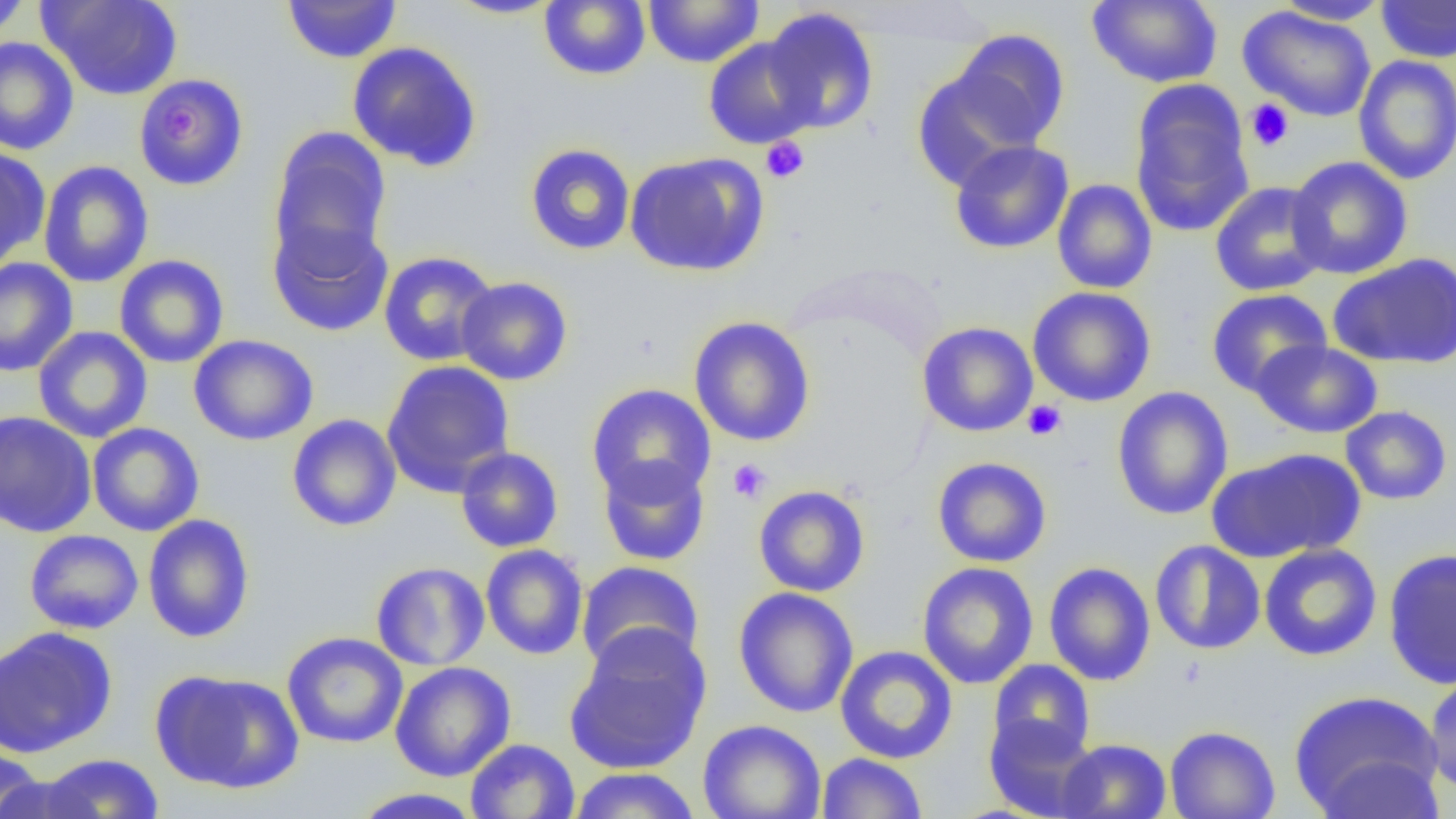

slide-level diagnosis = negative for blood parasites
magnification = 1000x
image size = 1456×819 pixels
field of view = one of a larger specimen
modality = optical microscopy
preparation = thin blood smear
platelet locations = approximate bounding boxes as named x1/y1/x2/y2 corners in pixels: (x1=1245, y1=99, x2=1295, y2=151), (x1=159, y1=104, x2=209, y2=140), (x1=761, y1=136, x2=810, y2=184), (x1=1023, y1=400, x2=1067, y2=441), (x1=727, y1=459, x2=773, y2=504)
uninfected red blood cell locations = approximate bounding boxes as named x1/y1/x2/y2 corners in pixels: (x1=0, y1=0, x2=32, y2=40), (x1=40, y1=0, x2=182, y2=101), (x1=445, y1=0, x2=562, y2=19), (x1=643, y1=0, x2=764, y2=67), (x1=1087, y1=0, x2=1223, y2=88), (x1=1273, y1=0, x2=1392, y2=25), (x1=1375, y1=0, x2=1456, y2=62), (x1=282, y1=1, x2=403, y2=64), (x1=539, y1=1, x2=651, y2=81), (x1=1238, y1=6, x2=1377, y2=122), (x1=762, y1=7, x2=880, y2=134), (x1=949, y1=29, x2=1071, y2=149), (x1=0, y1=37, x2=79, y2=155), (x1=703, y1=37, x2=817, y2=149), (x1=347, y1=41, x2=483, y2=172), (x1=1352, y1=55, x2=1456, y2=185), (x1=912, y1=67, x2=1037, y2=190), (x1=134, y1=73, x2=249, y2=191), (x1=1129, y1=82, x2=1255, y2=237), (x1=267, y1=125, x2=392, y2=270), (x1=949, y1=139, x2=1074, y2=254), (x1=524, y1=143, x2=636, y2=255), (x1=0, y1=148, x2=51, y2=267), (x1=624, y1=152, x2=768, y2=277), (x1=1286, y1=156, x2=1414, y2=279), (x1=38, y1=160, x2=154, y2=288), (x1=1052, y1=178, x2=1157, y2=294), (x1=1210, y1=181, x2=1330, y2=297), (x1=267, y1=218, x2=394, y2=338), (x1=378, y1=251, x2=500, y2=366), (x1=1329, y1=253, x2=1456, y2=369), (x1=114, y1=254, x2=230, y2=368), (x1=0, y1=257, x2=79, y2=376), (x1=455, y1=276, x2=573, y2=386), (x1=1028, y1=286, x2=1156, y2=407), (x1=1206, y1=288, x2=1333, y2=397), (x1=688, y1=316, x2=816, y2=447), (x1=917, y1=321, x2=1038, y2=437), (x1=32, y1=326, x2=153, y2=443), (x1=189, y1=335, x2=318, y2=445), (x1=1251, y1=340, x2=1383, y2=439), (x1=381, y1=360, x2=516, y2=497), (x1=586, y1=383, x2=716, y2=503), (x1=1112, y1=386, x2=1234, y2=520), (x1=1340, y1=405, x2=1453, y2=505), (x1=0, y1=410, x2=97, y2=538), (x1=286, y1=414, x2=402, y2=531), (x1=87, y1=422, x2=204, y2=536), (x1=455, y1=447, x2=564, y2=553), (x1=1207, y1=447, x2=1366, y2=563), (x1=597, y1=454, x2=711, y2=566), (x1=932, y1=456, x2=1052, y2=567), (x1=753, y1=485, x2=870, y2=597), (x1=142, y1=514, x2=255, y2=643), (x1=23, y1=529, x2=144, y2=634), (x1=1150, y1=540, x2=1265, y2=655), (x1=1259, y1=543, x2=1382, y2=661), (x1=480, y1=544, x2=589, y2=660), (x1=1383, y1=548, x2=1456, y2=689), (x1=370, y1=561, x2=490, y2=671), (x1=576, y1=561, x2=705, y2=673), (x1=1043, y1=561, x2=1156, y2=686), (x1=917, y1=562, x2=1039, y2=689), (x1=733, y1=587, x2=859, y2=718), (x1=564, y1=625, x2=712, y2=774), (x1=0, y1=626, x2=117, y2=758), (x1=282, y1=631, x2=408, y2=749), (x1=834, y1=646, x2=958, y2=764), (x1=987, y1=659, x2=1096, y2=762), (x1=390, y1=661, x2=516, y2=781), (x1=151, y1=669, x2=305, y2=795), (x1=1423, y1=673, x2=1456, y2=798), (x1=1289, y1=689, x2=1444, y2=818), (x1=984, y1=714, x2=1100, y2=819), (x1=697, y1=719, x2=827, y2=819), (x1=1165, y1=725, x2=1280, y2=819), (x1=465, y1=738, x2=580, y2=819), (x1=1056, y1=738, x2=1172, y2=819), (x1=0, y1=747, x2=44, y2=819), (x1=817, y1=752, x2=927, y2=818), (x1=38, y1=753, x2=164, y2=818), (x1=1313, y1=755, x2=1446, y2=818), (x1=568, y1=767, x2=701, y2=819), (x1=0, y1=774, x2=104, y2=819), (x1=349, y1=787, x2=485, y2=818)